Locate and identify every blood parasite.
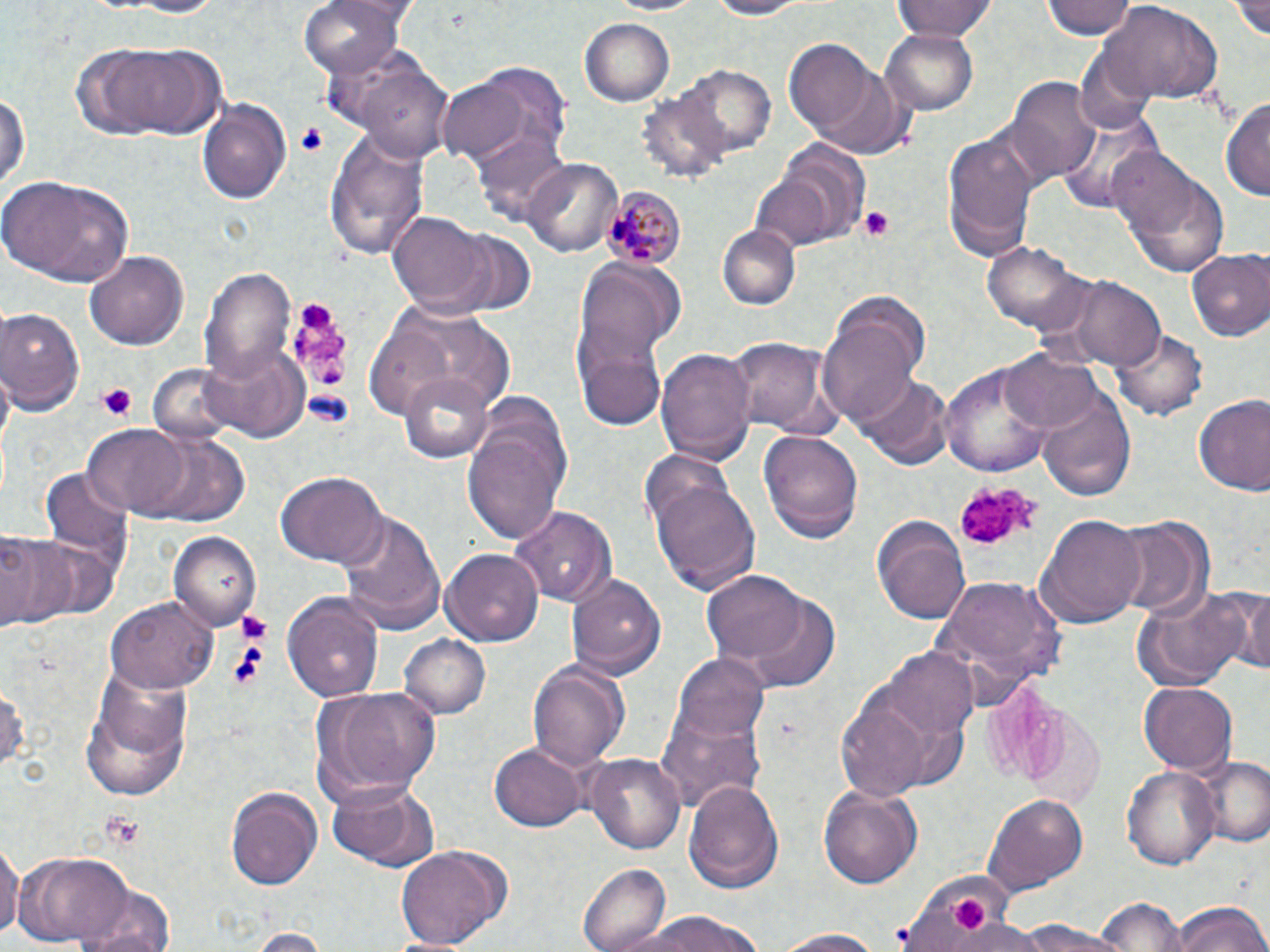
Approximate bounding boxes as named x1/y1/x2/y2 corners in pixels.
Plasmodium malariae-infected red blood cells: (x1=606, y1=185, x2=685, y2=269).
No Plasmodium falciparum, Plasmodium ovale, Plasmodium vivax, Babesia divergens, or Trypanosoma brucei observed.

Uninfected red blood cell locations: (x1=101, y1=0, x2=231, y2=18), (x1=301, y1=0, x2=406, y2=80), (x1=600, y1=0, x2=715, y2=17), (x1=694, y1=0, x2=815, y2=19), (x1=894, y1=0, x2=995, y2=43), (x1=1043, y1=0, x2=1134, y2=41), (x1=1230, y1=0, x2=1270, y2=42), (x1=1099, y1=3, x2=1224, y2=107), (x1=579, y1=15, x2=674, y2=103), (x1=881, y1=28, x2=979, y2=115), (x1=785, y1=39, x2=877, y2=136), (x1=84, y1=41, x2=230, y2=139), (x1=356, y1=63, x2=455, y2=163), (x1=679, y1=63, x2=778, y2=156), (x1=810, y1=68, x2=916, y2=158), (x1=437, y1=71, x2=553, y2=167), (x1=1008, y1=74, x2=1102, y2=181), (x1=0, y1=86, x2=28, y2=194), (x1=641, y1=88, x2=737, y2=186), (x1=197, y1=95, x2=291, y2=205), (x1=1221, y1=97, x2=1270, y2=203), (x1=1059, y1=107, x2=1163, y2=215), (x1=944, y1=126, x2=1036, y2=257), (x1=322, y1=130, x2=428, y2=264), (x1=473, y1=130, x2=572, y2=228), (x1=771, y1=137, x2=871, y2=244), (x1=1112, y1=153, x2=1227, y2=277), (x1=523, y1=158, x2=622, y2=256), (x1=751, y1=171, x2=837, y2=251), (x1=2, y1=173, x2=135, y2=287), (x1=389, y1=212, x2=491, y2=313), (x1=718, y1=225, x2=800, y2=309), (x1=431, y1=228, x2=537, y2=319), (x1=982, y1=242, x2=1094, y2=339), (x1=84, y1=249, x2=186, y2=351), (x1=1186, y1=250, x2=1270, y2=342), (x1=573, y1=255, x2=683, y2=405), (x1=201, y1=264, x2=295, y2=382), (x1=1050, y1=272, x2=1166, y2=370), (x1=0, y1=307, x2=85, y2=414), (x1=368, y1=307, x2=507, y2=419), (x1=818, y1=317, x2=920, y2=428), (x1=1113, y1=325, x2=1209, y2=421), (x1=724, y1=337, x2=840, y2=437), (x1=203, y1=345, x2=309, y2=443), (x1=656, y1=346, x2=755, y2=464), (x1=580, y1=349, x2=665, y2=430), (x1=1001, y1=350, x2=1103, y2=435), (x1=941, y1=360, x2=1055, y2=475), (x1=145, y1=362, x2=242, y2=447), (x1=401, y1=372, x2=495, y2=464), (x1=852, y1=374, x2=952, y2=470), (x1=1036, y1=383, x2=1135, y2=501), (x1=1190, y1=394, x2=1270, y2=497), (x1=464, y1=423, x2=566, y2=545), (x1=84, y1=424, x2=188, y2=514), (x1=759, y1=427, x2=864, y2=542), (x1=143, y1=434, x2=247, y2=526), (x1=42, y1=466, x2=134, y2=569), (x1=275, y1=471, x2=386, y2=567), (x1=649, y1=480, x2=761, y2=594), (x1=508, y1=504, x2=618, y2=609), (x1=338, y1=509, x2=446, y2=634), (x1=873, y1=514, x2=970, y2=622), (x1=1040, y1=514, x2=1147, y2=626), (x1=1110, y1=514, x2=1214, y2=620), (x1=171, y1=531, x2=260, y2=631), (x1=0, y1=533, x2=80, y2=634), (x1=443, y1=548, x2=546, y2=645), (x1=702, y1=570, x2=810, y2=668), (x1=567, y1=572, x2=665, y2=680), (x1=931, y1=572, x2=1071, y2=696), (x1=1234, y1=584, x2=1270, y2=676), (x1=1130, y1=586, x2=1253, y2=690), (x1=282, y1=591, x2=385, y2=702), (x1=744, y1=591, x2=841, y2=689), (x1=109, y1=598, x2=217, y2=695), (x1=400, y1=634, x2=491, y2=720), (x1=884, y1=648, x2=979, y2=742), (x1=672, y1=651, x2=769, y2=748), (x1=526, y1=660, x2=630, y2=771), (x1=78, y1=671, x2=194, y2=801), (x1=0, y1=677, x2=27, y2=778), (x1=833, y1=680, x2=945, y2=802), (x1=1138, y1=683, x2=1236, y2=773), (x1=307, y1=684, x2=442, y2=804), (x1=657, y1=700, x2=769, y2=812), (x1=488, y1=742, x2=588, y2=830), (x1=585, y1=752, x2=687, y2=854), (x1=1194, y1=755, x2=1270, y2=849), (x1=1122, y1=763, x2=1222, y2=872), (x1=326, y1=777, x2=437, y2=870), (x1=684, y1=777, x2=785, y2=894), (x1=816, y1=783, x2=920, y2=891), (x1=226, y1=784, x2=323, y2=891), (x1=985, y1=792, x2=1087, y2=892), (x1=0, y1=840, x2=20, y2=941), (x1=395, y1=842, x2=508, y2=951), (x1=20, y1=851, x2=132, y2=946), (x1=579, y1=861, x2=670, y2=952), (x1=899, y1=866, x2=1013, y2=948), (x1=65, y1=872, x2=177, y2=952), (x1=1093, y1=896, x2=1186, y2=952), (x1=1169, y1=900, x2=1270, y2=951), (x1=619, y1=911, x2=773, y2=952), (x1=943, y1=919, x2=1046, y2=952), (x1=246, y1=928, x2=330, y2=951), (x1=771, y1=928, x2=893, y2=951). Platelet locations: (x1=298, y1=122, x2=329, y2=157), (x1=858, y1=205, x2=899, y2=242), (x1=284, y1=296, x2=359, y2=399), (x1=97, y1=382, x2=138, y2=424), (x1=957, y1=480, x2=1042, y2=551), (x1=237, y1=607, x2=273, y2=644), (x1=226, y1=642, x2=268, y2=691), (x1=98, y1=811, x2=148, y2=847), (x1=947, y1=895, x2=989, y2=932). Slide-level diagnosis: Plasmodium malariae. Image is 1270×952 pixels. Single field of view. Thin blood smear. 1000x magnification. May-Grünwald-Giemsa-stained preparation. Light microscopy.